Classify this cell by malaria status.
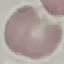

It is uninfected.

stain = Giemsa
preparation = thin blood film
image type = cell patch, automatically extracted from a larger field of view and resized to 64 × 64 pixels
capture = smartphone camera at the microscope eyepiece